Evaluate for Plasmodium parasites.
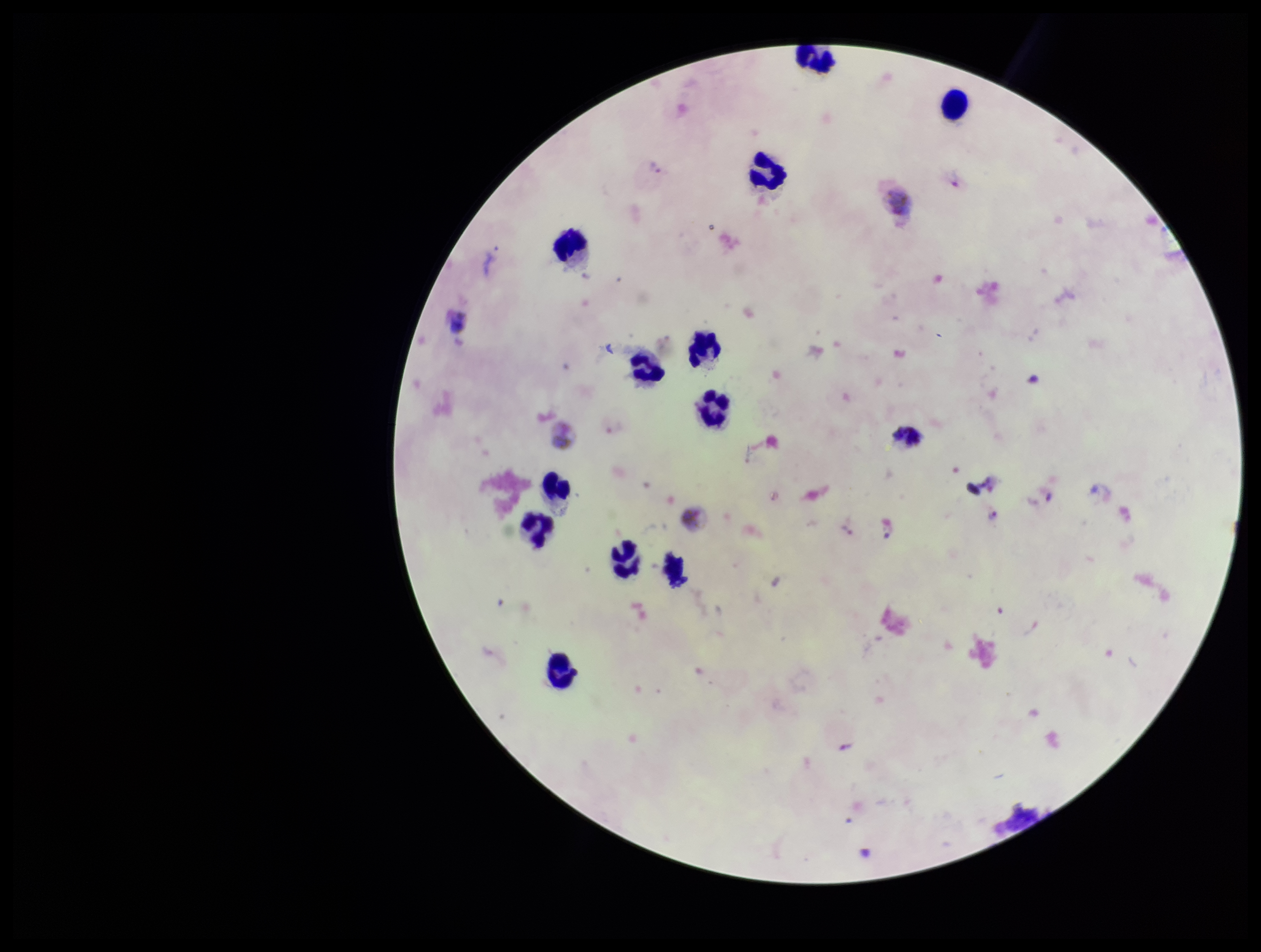

Identified.

patient malaria status = infected
image size = 1261×952 pixels
parasite count = 4
capture = smartphone photograph through the microscope eyepiece
stain = Giemsa
field of view = single
leukocyte count = 13
preparation = thick
species reported for this patient = Plasmodium vivax